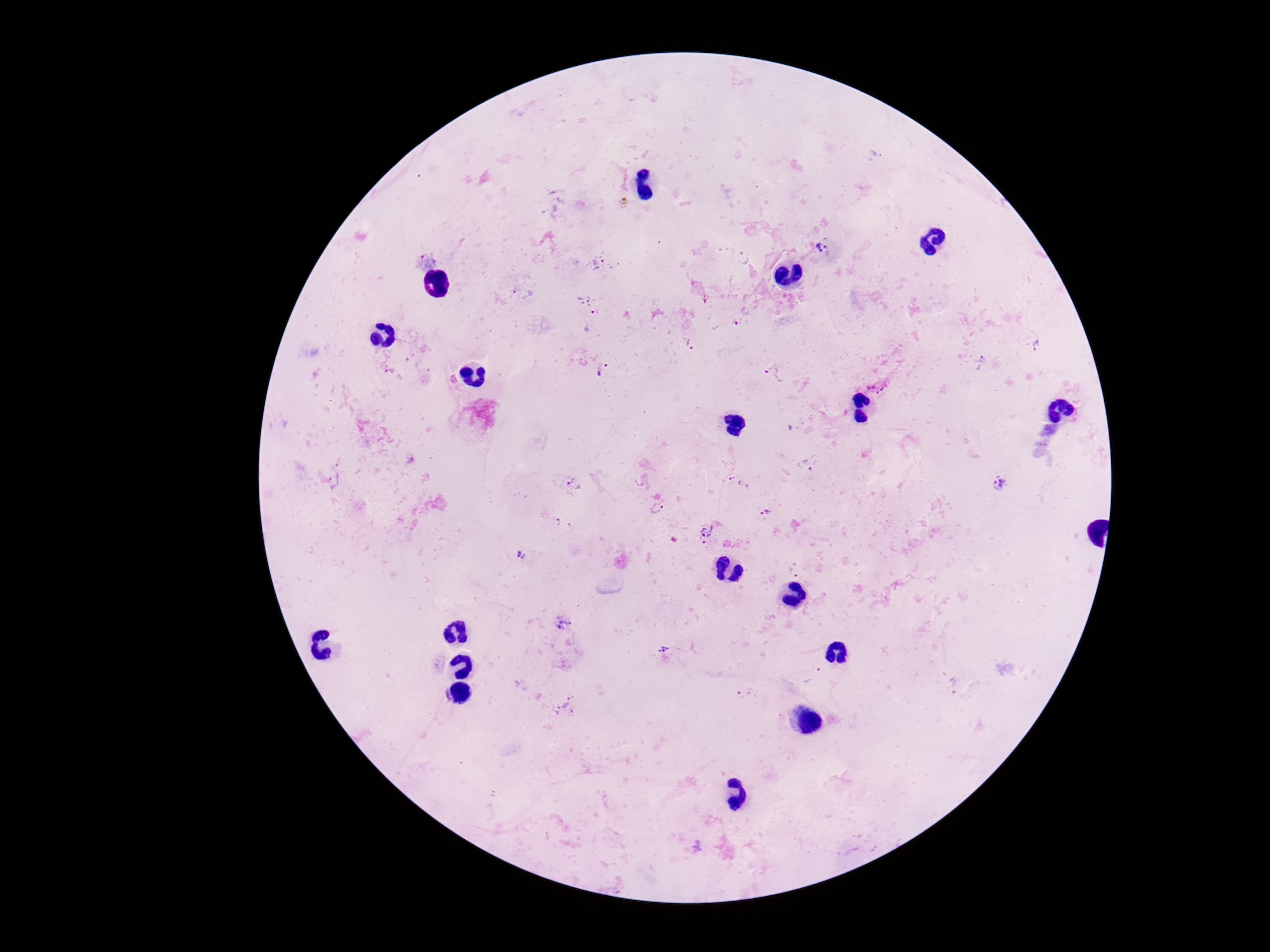

magnification = 100x
Plasmodium parasite locations = approximate object centers, in pixels from the top-left corner: (x=824, y=248), (x=742, y=257), (x=597, y=262), (x=583, y=298), (x=597, y=314), (x=689, y=343), (x=1039, y=347), (x=981, y=363), (x=602, y=369), (x=390, y=371), (x=773, y=375), (x=878, y=384), (x=809, y=462), (x=734, y=482), (x=575, y=484), (x=1000, y=484), (x=657, y=508), (x=765, y=512), (x=563, y=524), (x=707, y=533), (x=519, y=555), (x=796, y=569), (x=563, y=625), (x=665, y=647), (x=812, y=675), (x=746, y=693), (x=566, y=704)
capture = smartphone camera through the microscope eyepiece
stain = Giemsa
image size = 1270×952 pixels
preparation = thick blood film
field of view = one from this slide
patient malaria status = infected